Name the parasite shown.
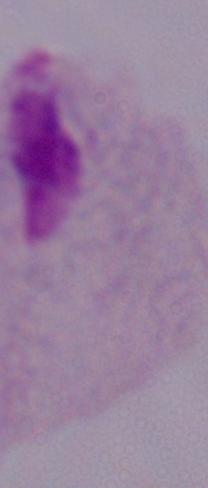

This is a trichomonad.

modality: micrograph
magnification: 1000x